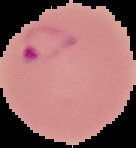

Summary:
  - Image size: 136×148 pixels
  - Result: malaria parasites identified
  - Image type: cell region segmented out of the field of view; surrounding area masked to black
  - Preparation: thin blood smear